Locate and identify every blood parasite.
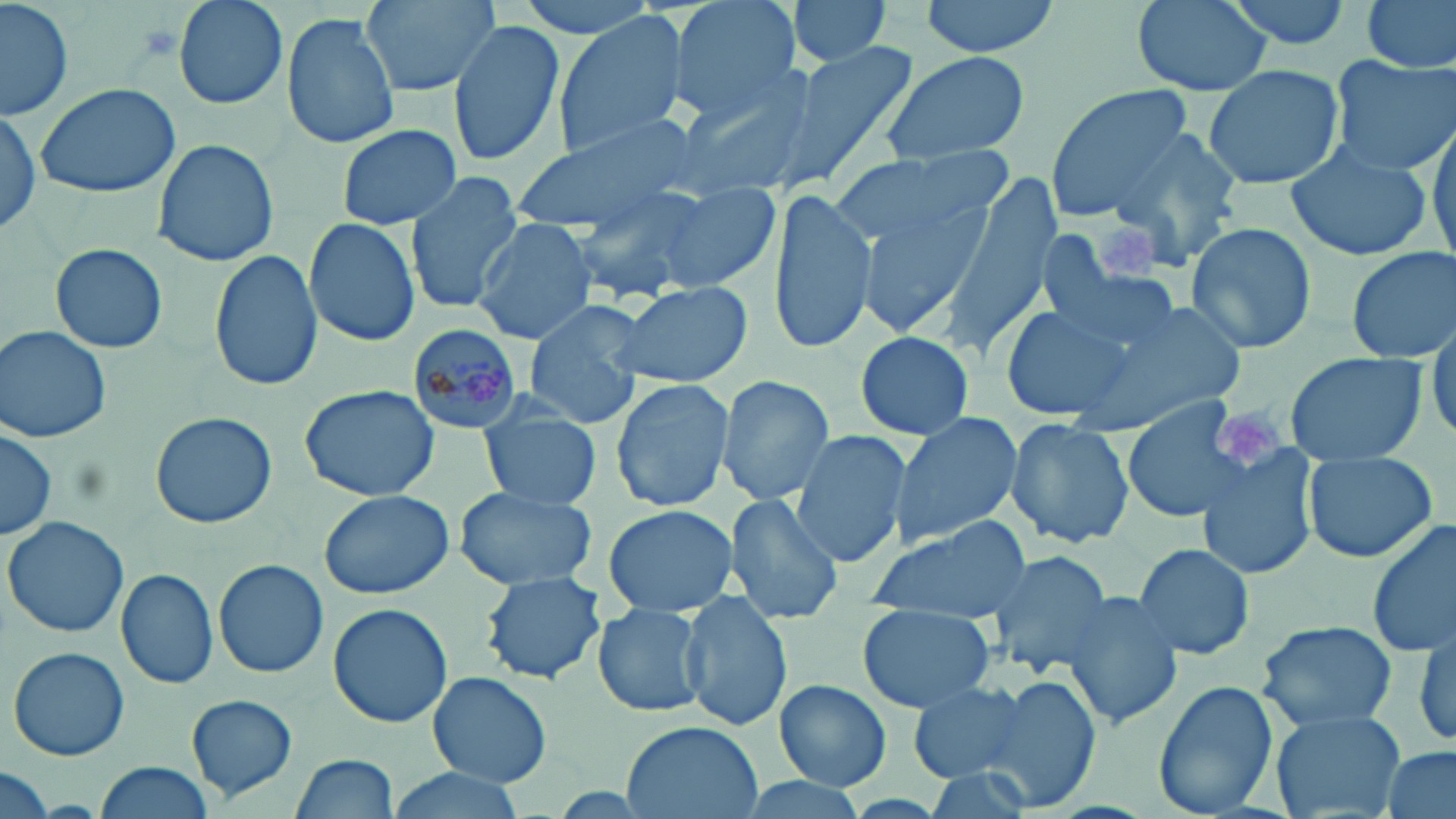
Approximate bounding boxes as (x1,y1)-(x2,y2) corner pairs in pixels.
Plasmodium malariae-infected red blood cells: (408,324)-(526,435).
No Plasmodium falciparum, Plasmodium ovale, Plasmodium vivax, Babesia divergens, or Trypanosoma brucei observed.

{
  "slide_level_diagnosis": "Plasmodium malariae",
  "uninfected_red_blood_cell_locations": "approximate bounding boxes as (x1,y1)-(x2,y2) corner pairs in pixels: (1,0)-(73,123), (171,0)-(289,110), (363,0)-(495,98), (515,0)-(665,39), (667,0)-(799,121), (785,0)-(893,66), (917,0)-(1065,54), (1131,0)-(1272,96), (1221,0)-(1355,51), (1357,0)-(1456,76), (551,11)-(691,157), (281,14)-(401,149), (447,18)-(565,167), (774,37)-(921,191), (878,51)-(1029,167), (1326,57)-(1456,176), (1203,64)-(1345,191), (671,73)-(820,202), (33,81)-(182,200), (1045,85)-(1196,218), (0,106)-(41,239), (1428,117)-(1456,263), (509,119)-(708,233), (336,121)-(461,230), (1110,126)-(1245,269), (153,136)-(278,266), (1284,138)-(1435,262), (831,145)-(1008,269), (944,172)-(1060,353), (404,173)-(523,314), (844,181)-(989,341), (563,184)-(718,302), (646,184)-(782,292), (767,188)-(877,356), (304,215)-(420,348), (472,217)-(596,343), (1184,221)-(1317,356), (46,243)-(171,355), (1345,244)-(1456,362), (209,249)-(324,394), (1041,259)-(1183,360), (609,280)-(753,389), (1104,296)-(1251,424), (523,300)-(651,429), (1001,305)-(1137,423), (1428,319)-(1456,441), (1,325)-(113,443), (853,330)-(976,442), (1280,349)-(1430,466), (716,375)-(836,506), (610,378)-(734,512), (297,384)-(440,500), (1119,399)-(1262,524), (479,404)-(602,511), (150,411)-(276,530), (887,412)-(1023,546), (1003,418)-(1134,547), (1,425)-(59,541), (792,431)-(911,569), (1199,444)-(1320,581), (1302,451)-(1438,565), (453,486)-(598,593), (317,487)-(458,600), (724,493)-(844,624), (600,503)-(739,617), (3,516)-(130,639), (1366,516)-(1456,658), (864,519)-(1032,621), (1131,542)-(1255,661), (985,549)-(1116,678), (212,559)-(329,679), (116,569)-(219,690), (482,574)-(606,683), (1058,590)-(1184,730), (681,594)-(793,731), (328,603)-(453,727), (592,604)-(707,718), (857,604)-(996,712), (1259,620)-(1399,734), (1408,627)-(1456,752), (7,645)-(131,761), (427,671)-(553,787), (980,674)-(1098,815), (772,679)-(892,791), (907,679)-(1029,782), (1153,680)-(1279,815), (187,694)-(298,801), (1269,709)-(1408,819), (620,720)-(765,818), (1381,747)-(1454,819), (292,755)-(400,818), (96,760)-(214,818), (916,765)-(1043,819), (0,767)-(57,819), (381,770)-(530,819), (733,777)-(878,819)",
  "image_size": "1456×819 pixels",
  "platelet_locations": "approximate bounding boxes as (x1,y1)-(x2,y2) corner pairs in pixels: (1099,219)-(1158,277), (1216,400)-(1283,465)",
  "magnification": "1000x",
  "modality": "light microscopy",
  "field_of_view": "one of a larger specimen",
  "stain": "May-Grünwald-Giemsa",
  "preparation": "thin blood film"
}